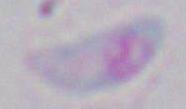
magnification = 1000x
modality = micrograph
identification = Toxoplasma gondii